Describe the morphology of the red blood cells.
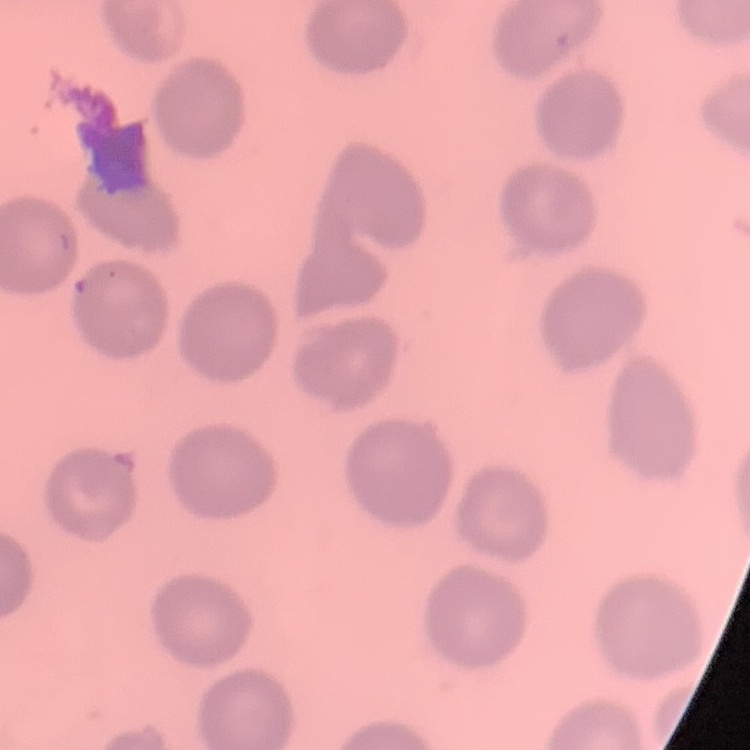
No rouleaux formation.

Summary:
  - Preparation: thin blood smear
  - Image type: one tile cut from a larger photomicrograph
  - Stain: Field's or Giemsa